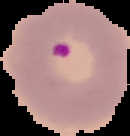

result: Plasmodium parasites detected
image_size: 130×136 pixels
image_type: cell region segmented out of the field of view; surrounding area masked to black
preparation: thin blood film